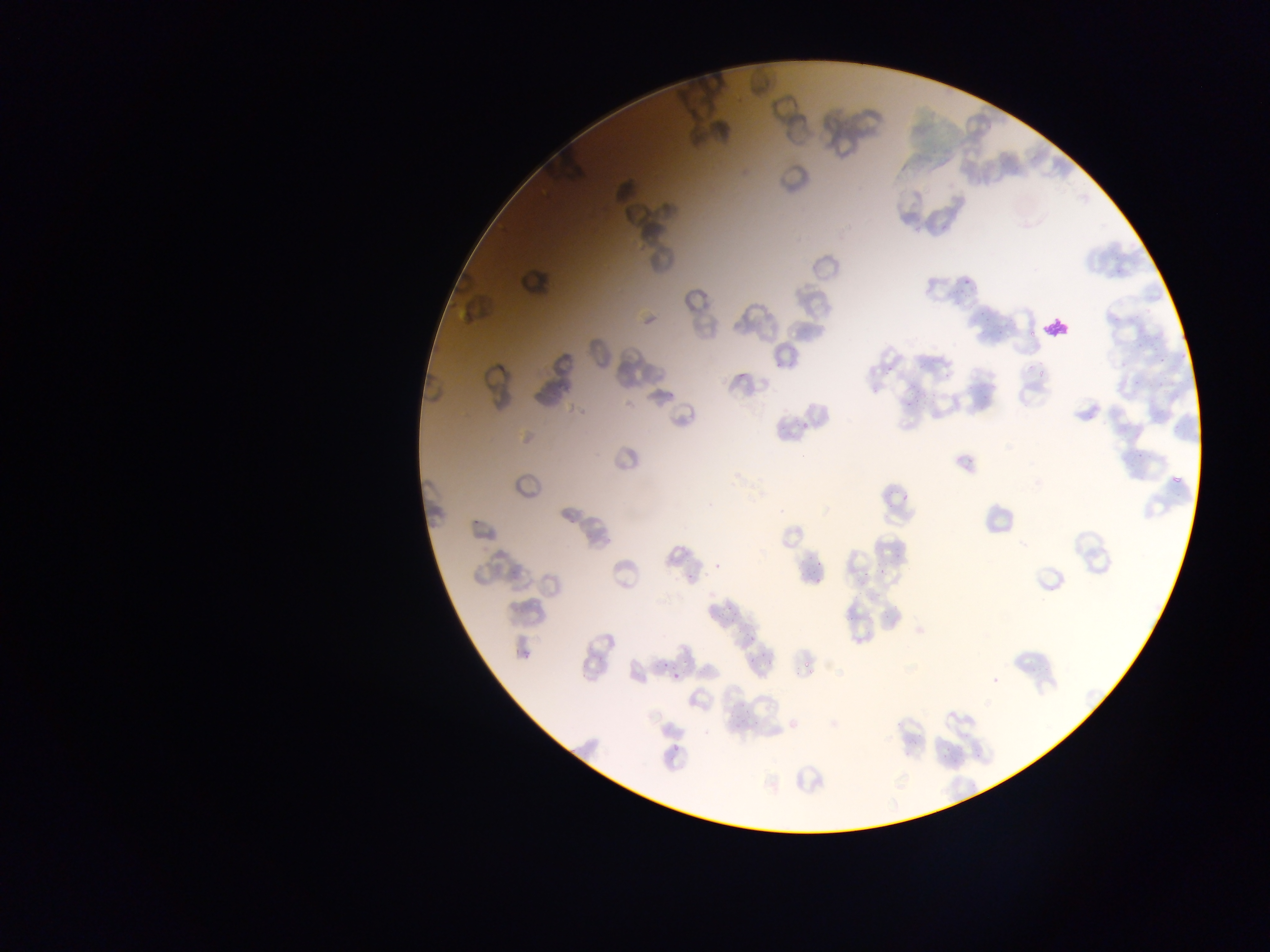 Approximate bounding boxes as (left, top, right, bottom) in pixels. Malaria parasite locations: (962, 268, 979, 289), (1167, 471, 1186, 491), (710, 559, 722, 569), (739, 628, 751, 639), (657, 656, 668, 671), (671, 668, 683, 679), (671, 737, 682, 755). Leukocyte locations: (1039, 314, 1075, 345). Mobile-phone photograph taken through the microscope. Collected in Ghana. Single field of view. Image is 1270×952 pixels. Thin blood smear.